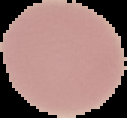 Image is 127×118 pixels. Result: no malaria parasites detected. Cell region segmented out of the field of view; the surrounding area is masked to black. From a thin blood smear.